Classify this cell by malaria status.
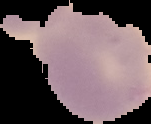

It is uninfected.

Summary:
  - Preparation: thin blood smear
  - Image size: 151×124 pixels
  - Image type: segmented cell region on a black background